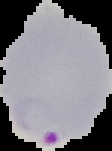

Summary:
  - Preparation: thin blood smear
  - Malaria status: parasitized
  - Image size: 112×151 pixels
  - Image type: segmented cell region on a black background